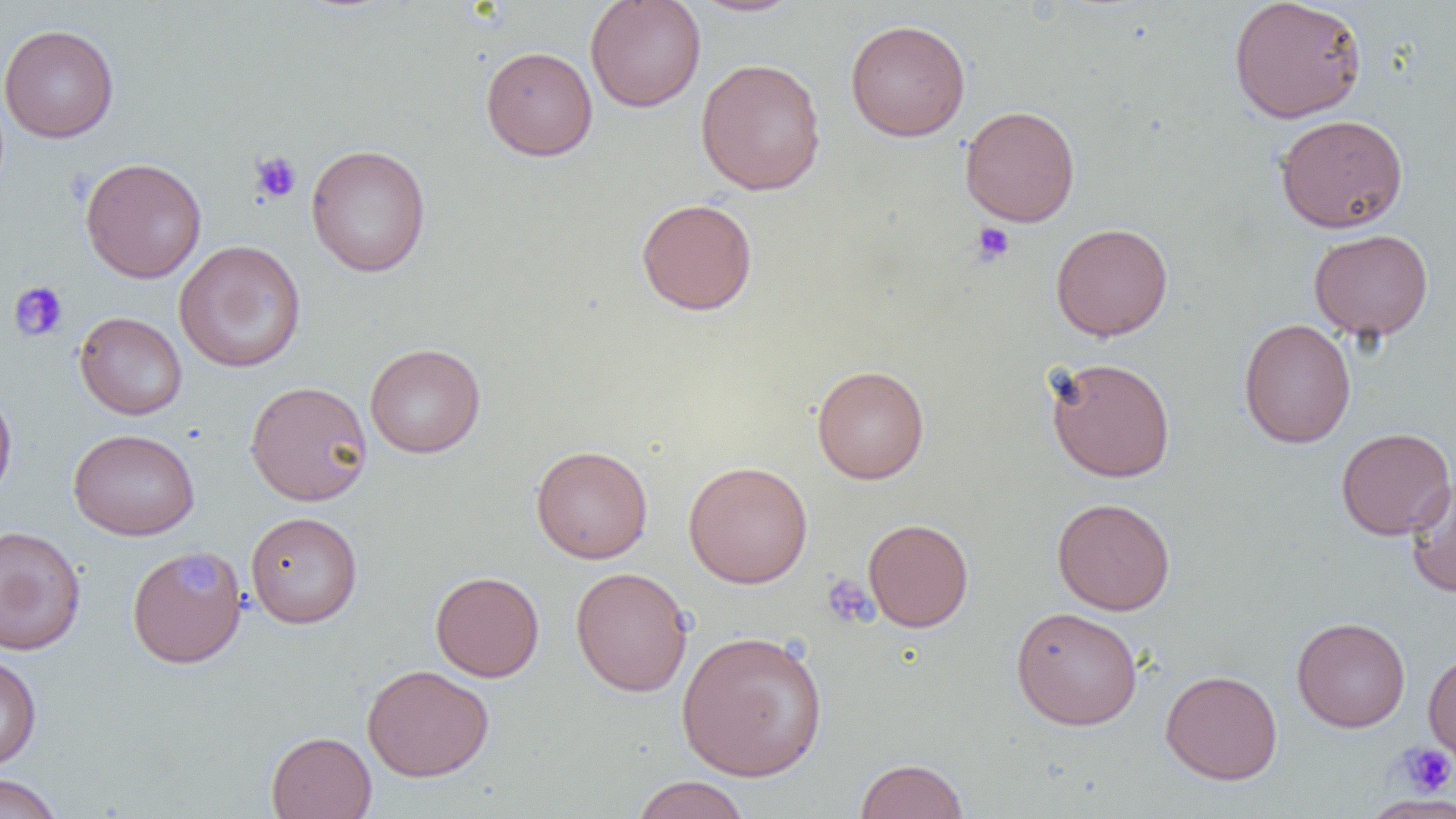

Approximate bounding boxes as (x1, y1, x2, y2) in pixels. Platelet locations: (249, 150, 302, 204), (971, 222, 1016, 265), (8, 280, 68, 342), (180, 556, 215, 596), (820, 573, 878, 629), (1396, 741, 1456, 797). Uninfected red blood cell locations: (585, 0, 706, 112), (690, 0, 805, 17), (1228, 0, 1367, 124), (845, 18, 971, 142), (0, 24, 119, 143), (481, 45, 598, 161), (695, 58, 826, 196), (960, 105, 1080, 227), (1274, 114, 1409, 233), (305, 143, 432, 277), (80, 157, 207, 283), (636, 198, 758, 315), (1050, 222, 1174, 340), (1308, 229, 1434, 341), (174, 240, 306, 373), (74, 311, 188, 420), (1239, 318, 1356, 448), (365, 343, 486, 458), (1044, 356, 1176, 482), (812, 365, 930, 484), (245, 380, 373, 506), (0, 384, 17, 506), (1336, 426, 1455, 540), (68, 428, 200, 540), (531, 444, 653, 563), (683, 460, 813, 588), (1404, 473, 1456, 597), (1051, 497, 1176, 615), (246, 511, 363, 628), (862, 518, 974, 632), (0, 524, 87, 656), (127, 548, 248, 667), (570, 567, 693, 697), (430, 570, 544, 682), (1011, 606, 1143, 729), (1291, 616, 1411, 732), (676, 629, 829, 781), (1423, 649, 1456, 766), (0, 654, 41, 771), (362, 664, 494, 782), (1160, 669, 1283, 785), (265, 731, 376, 819), (854, 757, 970, 819), (0, 774, 65, 819), (630, 775, 751, 819), (1361, 795, 1456, 818). Slide-level diagnosis: no evidence of blood parasites. Captured at 1000x magnification. Thin blood film. Single field of view. Optical microscopy. Image is 1456×819 pixels.